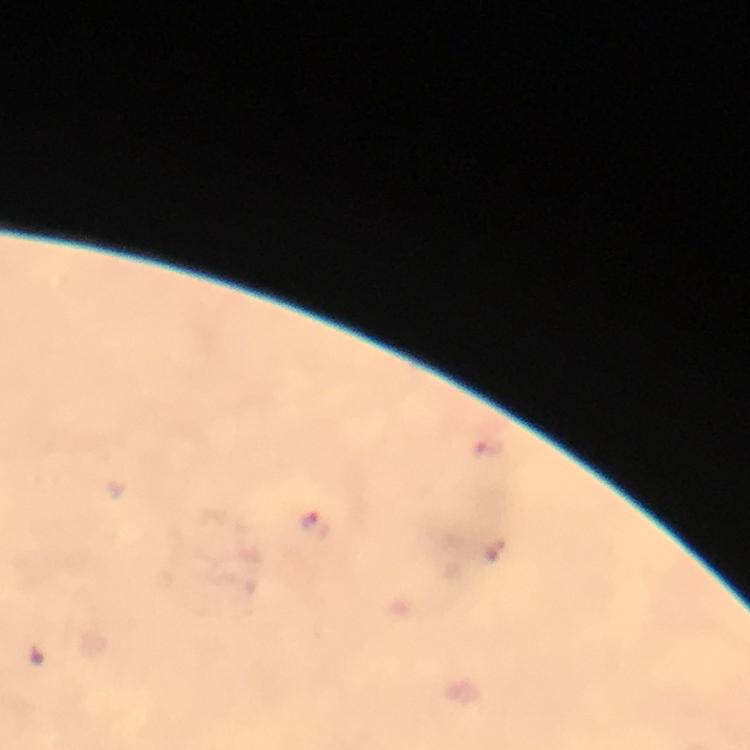
Approximate object centers, in pixels from the top-left corner.
Summary:
  - Plasmodium parasite locations: (x=312, y=526)
  - Image size: 750×750 pixels
  - Immersion oil: applied
  - Stain: Giemsa
  - Cropped from: a single field of view
  - Preparation: thick smear
  - Capture: smartphone mounted on the microscope
  - Magnification: 100x
  - Context: from a diagnostic examination for malaria